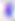

Toxoplasma gondii is seen. Photomicrograph. 400x magnification.